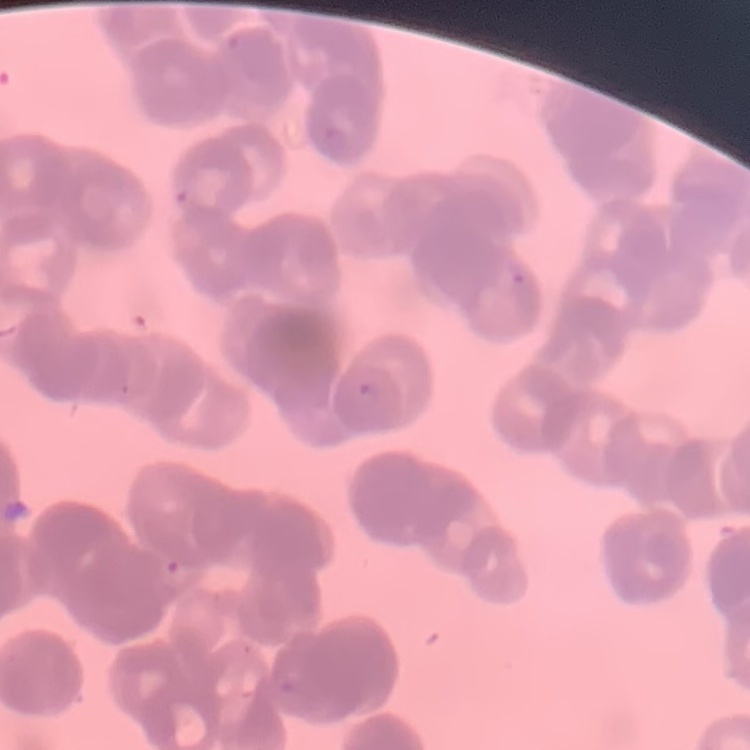
erythrocyte morphology = rouleaux formation
stain = Field's or Giemsa
preparation = thin blood smear
image type = square crop of a larger photomicrograph